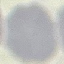

malaria status = uninfected
preparation = thin blood smear
stain = Giemsa
image type = automatically extracted cell patch, resized to 64 × 64 pixels
capture = smartphone through the microscope eyepiece